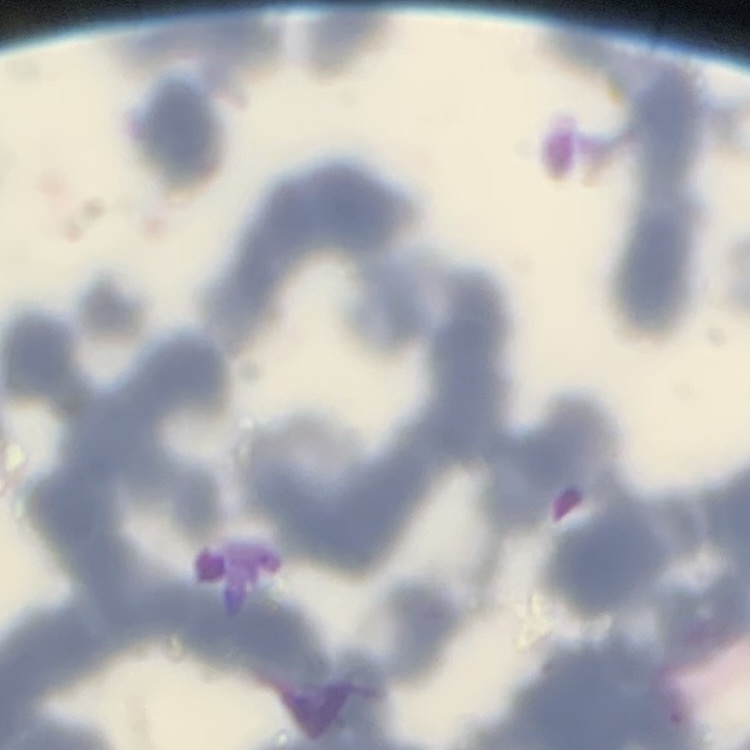
Summary:
  - Red blood cell morphology: rouleaux formation
  - Image type: square crop of a larger photomicrograph
  - Preparation: thin blood smear
  - Stain: Field's or Giemsa